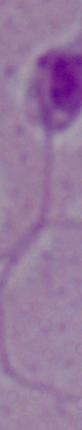

modality: photomicrograph
magnification: 1000x
identification: Leishmania